Name the parasite shown.
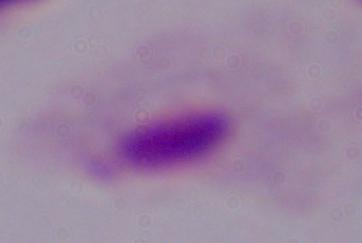

This is a trichomonad.

Summary:
  - Modality: photomicrograph
  - Magnification: 1000x